Classify this cell by malaria status.
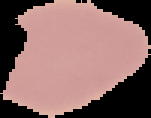
Uninfected.

image type = segmented cell region with the area outside set to black
image size = 151×118 pixels
preparation = thin blood smear